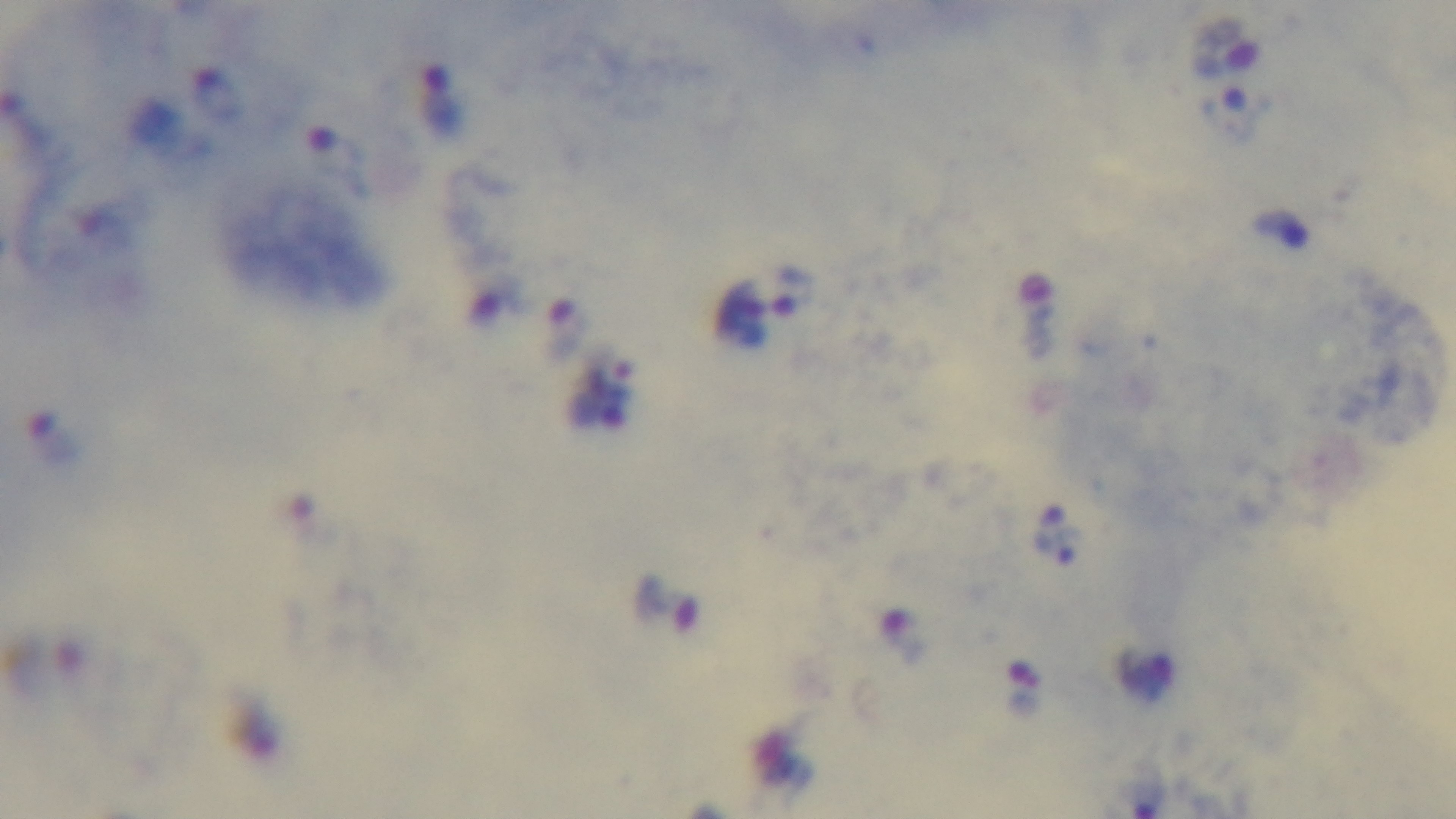

modality = light microscopy
preparation = thick smear
objective = 100x oil immersion
malaria status = positive
stain = Giemsa
capture = mounted 4K digital camera
field of view = single